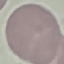
malaria status = uninfected
image type = cell patch, automatically extracted from a larger field of view and resized to 64 × 64 pixels
capture = smartphone camera at the microscope eyepiece
preparation = thin blood smear
stain = Giemsa